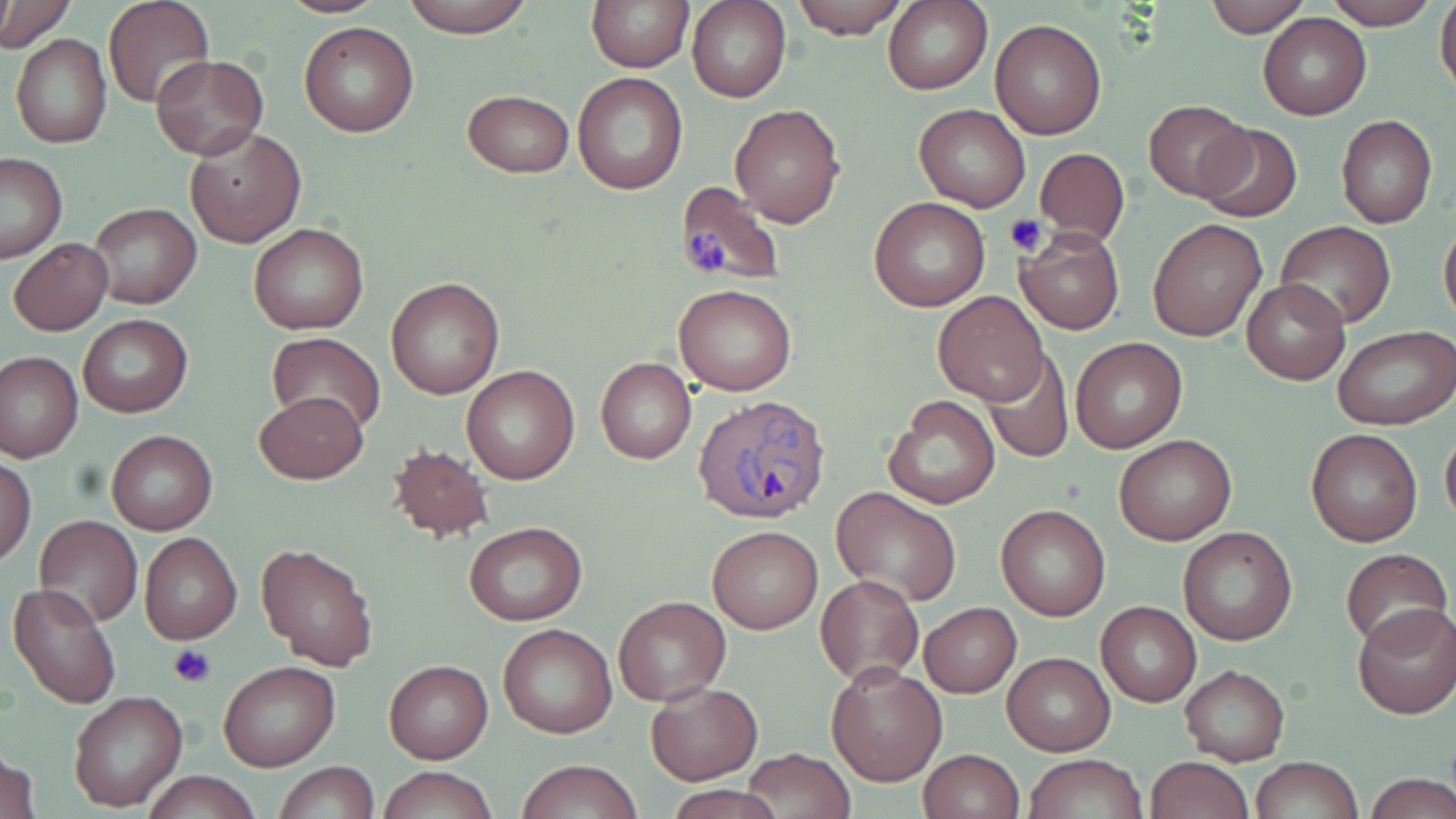
Summary:
  - Coordinate format: approximate bounding boxes as (x1,y1)-(x2,y2) corner pairs in pixels
  - Plasmodium ovale-infected red blood cell locations: (696,396)-(834,523)
  - Uninfected red blood cell locations: (1,0)-(72,52), (275,0)-(390,17), (398,0)-(538,36), (587,0)-(692,71), (688,0)-(791,103), (789,0)-(909,40), (885,0)-(994,96), (1204,0)-(1310,37), (1322,0)-(1439,29), (1434,0)-(1456,99), (104,1)-(213,109), (1258,14)-(1371,120), (990,18)-(1107,139), (300,21)-(419,137), (10,32)-(112,150), (152,54)-(268,159), (572,71)-(687,193), (462,89)-(574,177), (1143,99)-(1252,202), (729,103)-(845,226), (914,104)-(1030,212), (1336,115)-(1438,229), (1193,123)-(1303,222), (185,127)-(306,247), (1034,147)-(1129,247), (0,154)-(68,262), (672,179)-(786,288), (869,198)-(991,312), (86,203)-(201,311), (1439,217)-(1456,332), (1147,218)-(1267,341), (1277,221)-(1395,329), (248,222)-(369,335), (1013,227)-(1124,334), (8,237)-(111,335), (386,276)-(504,400), (1241,279)-(1349,385), (676,284)-(796,396), (932,290)-(1049,405), (78,314)-(192,417), (1335,327)-(1455,431), (266,333)-(385,438), (1071,337)-(1187,453), (0,351)-(82,461), (983,353)-(1073,463), (596,357)-(696,465), (460,364)-(579,484), (255,392)-(368,485), (881,393)-(1001,510), (1440,424)-(1456,532), (1306,428)-(1422,546), (105,430)-(218,534), (1114,432)-(1235,546), (386,442)-(494,543), (0,456)-(36,565), (830,488)-(963,607), (996,503)-(1110,621), (34,514)-(143,626), (465,521)-(587,625), (707,525)-(821,633), (1177,527)-(1298,647), (139,532)-(242,645), (255,541)-(379,670), (1340,547)-(1452,652), (816,575)-(924,685), (7,580)-(123,707), (613,596)-(729,705), (1097,601)-(1201,706), (919,602)-(1021,698), (1353,604)-(1456,719), (497,622)-(617,738), (1002,651)-(1115,756), (218,660)-(340,771), (385,660)-(492,764), (825,660)-(945,786), (1180,665)-(1289,765), (646,681)-(762,784), (68,690)-(188,811), (1,742)-(40,819), (742,748)-(856,819), (918,749)-(1023,819), (1025,753)-(1149,818), (1147,756)-(1253,819), (1251,756)-(1361,819), (517,759)-(641,819), (276,762)-(378,819), (379,766)-(495,819), (141,770)-(262,819), (1367,774)-(1456,819), (667,786)-(779,818)
  - Platelet locations: (1005,214)-(1048,256), (685,225)-(728,274), (169,644)-(215,687)
  - Slide-level diagnosis: Plasmodium ovale
  - Preparation: thin blood film
  - Image size: 1456×819 pixels
  - Modality: light microscopy
  - Magnification: 1000x
  - Field of view: single
  - Stain: May-Grünwald-Giemsa